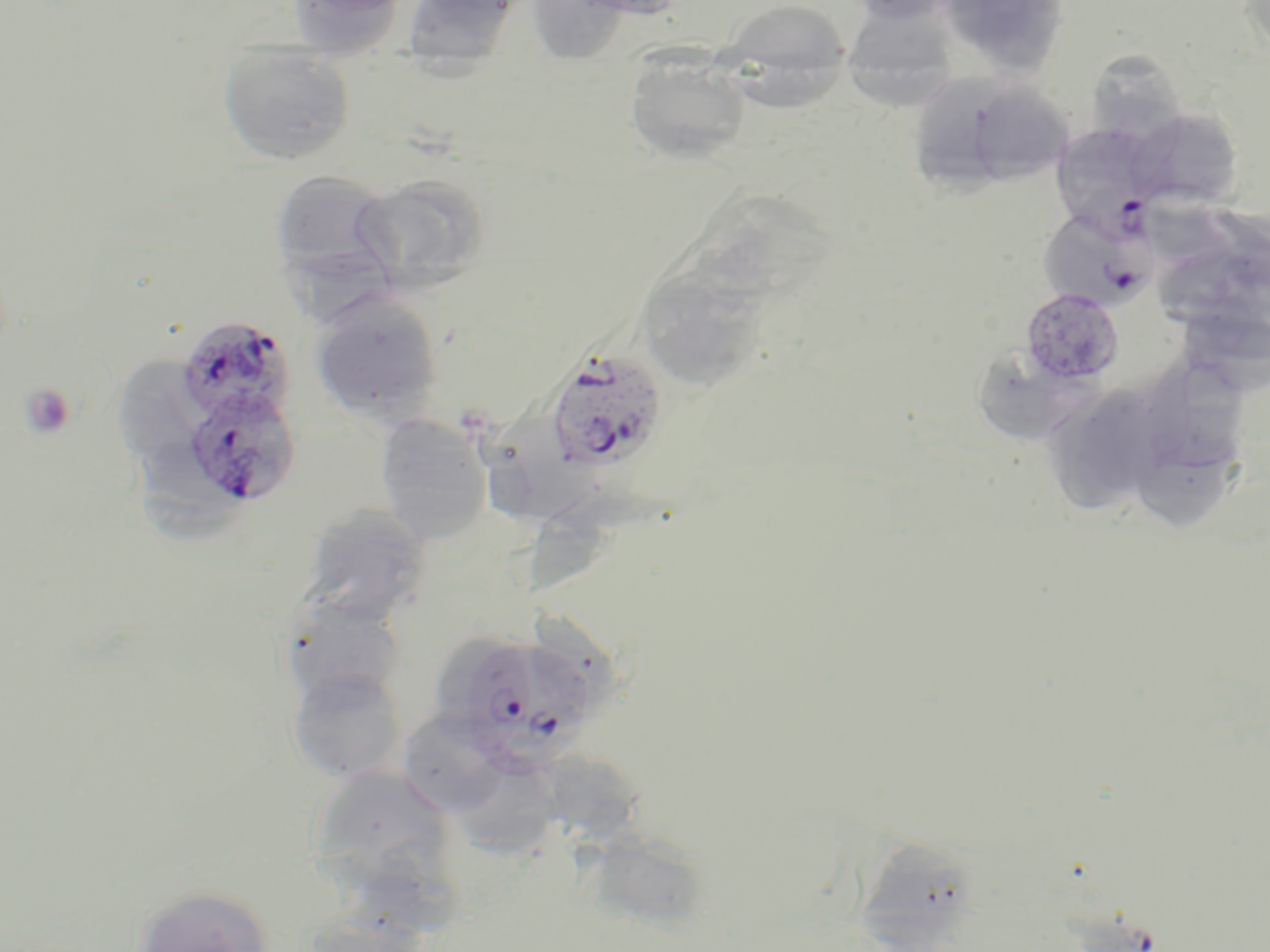

slide-level diagnosis = Plasmodium falciparum
preparation = thin blood film
platelet locations = approximate bounding boxes as named x1/y1/x2/y2 corners in pixels: (x1=19, y1=383, x2=77, y2=440)
magnification = 1000x
field of view = one of a larger specimen
stain = May-Grünwald-Giemsa
modality = light microscopy
Plasmodium falciparum-infected red blood cell locations = approximate bounding boxes as named x1/y1/x2/y2 corners in pixels: (x1=1051, y1=122, x2=1163, y2=233), (x1=1038, y1=208, x2=1157, y2=312), (x1=175, y1=314, x2=297, y2=426), (x1=545, y1=348, x2=668, y2=475), (x1=182, y1=387, x2=301, y2=509), (x1=445, y1=630, x2=597, y2=773)
image size = 1270×952 pixels
uninfected red blood cell locations = approximate bounding boxes as named x1/y1/x2/y2 corners in pixels: (x1=286, y1=0, x2=410, y2=59), (x1=401, y1=0, x2=521, y2=71), (x1=532, y1=0, x2=629, y2=63), (x1=715, y1=0, x2=853, y2=103), (x1=847, y1=0, x2=958, y2=25), (x1=978, y1=0, x2=1063, y2=74), (x1=846, y1=14, x2=958, y2=106), (x1=218, y1=42, x2=356, y2=165), (x1=1087, y1=50, x2=1187, y2=143), (x1=625, y1=52, x2=751, y2=165), (x1=911, y1=72, x2=1022, y2=204), (x1=979, y1=84, x2=1071, y2=182), (x1=1126, y1=108, x2=1244, y2=211), (x1=269, y1=167, x2=402, y2=293), (x1=358, y1=174, x2=491, y2=293), (x1=683, y1=190, x2=841, y2=307), (x1=1154, y1=201, x2=1239, y2=274), (x1=1160, y1=251, x2=1247, y2=329), (x1=638, y1=262, x2=771, y2=402), (x1=1021, y1=288, x2=1125, y2=385), (x1=309, y1=290, x2=444, y2=424), (x1=987, y1=356, x2=1089, y2=438), (x1=116, y1=358, x2=199, y2=457), (x1=1154, y1=365, x2=1239, y2=470), (x1=487, y1=401, x2=592, y2=524), (x1=1053, y1=402, x2=1154, y2=523), (x1=375, y1=413, x2=494, y2=544), (x1=140, y1=442, x2=248, y2=546), (x1=1145, y1=442, x2=1231, y2=531), (x1=522, y1=486, x2=631, y2=602), (x1=301, y1=503, x2=432, y2=623), (x1=279, y1=596, x2=410, y2=714), (x1=287, y1=667, x2=409, y2=784), (x1=400, y1=712, x2=514, y2=816), (x1=459, y1=747, x2=559, y2=857), (x1=553, y1=751, x2=654, y2=857), (x1=322, y1=770, x2=455, y2=885), (x1=583, y1=835, x2=702, y2=929), (x1=858, y1=835, x2=979, y2=952), (x1=352, y1=853, x2=465, y2=949), (x1=128, y1=883, x2=277, y2=952)